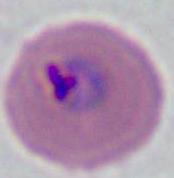
Photomicrograph. 400x or 1000x magnification. A Plasmodium parasite is shown.